Give the position of every Plasmodium parasite visible.
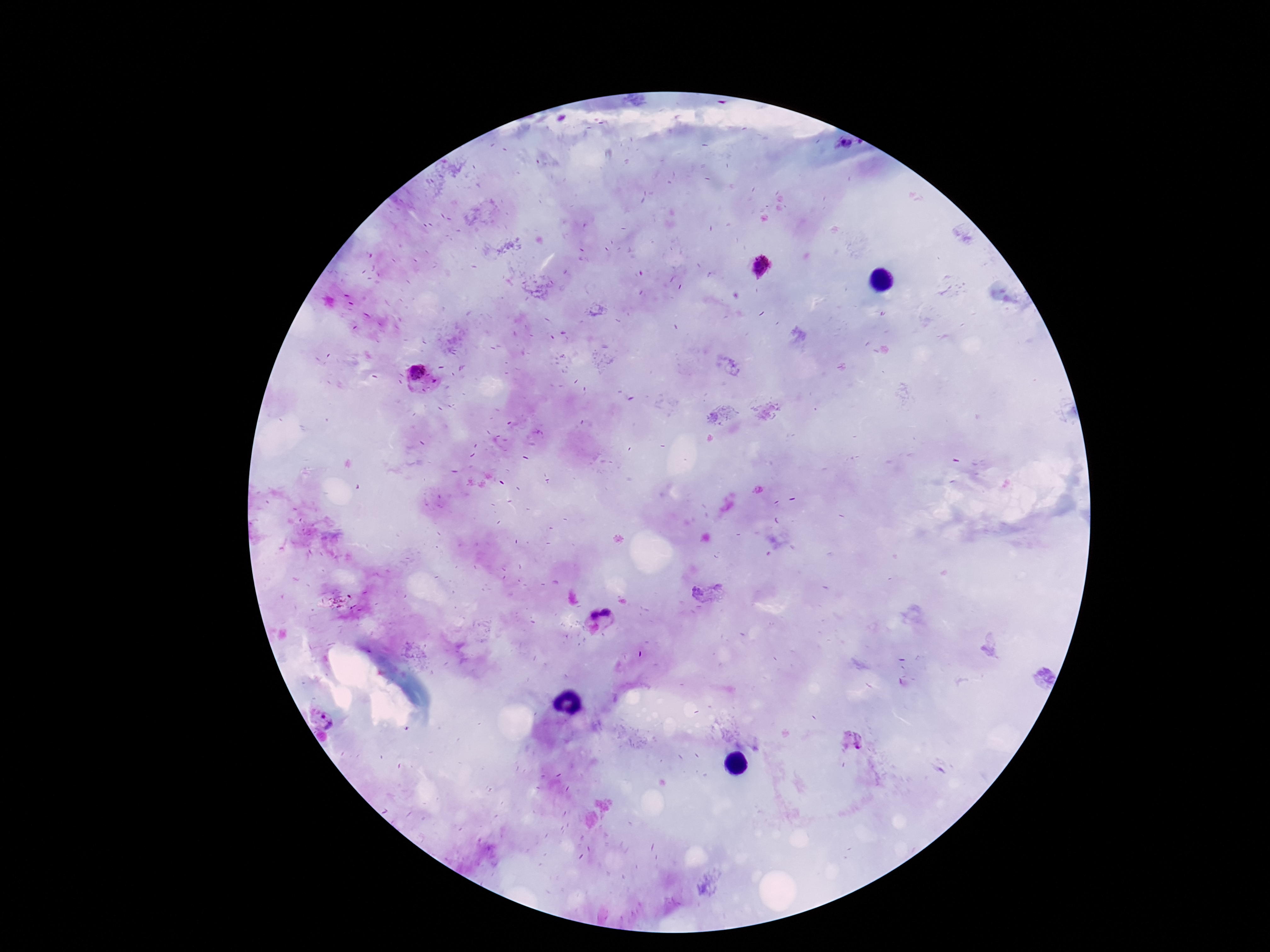
Approximate centers as (x, y) in pixels.
Plasmodium parasites: (845, 146), (761, 267), (419, 378), (705, 591), (608, 612), (593, 616), (1044, 679), (323, 720), (854, 740).

Summary:
  - Stain: Giemsa
  - Capture: smartphone camera through the microscope eyepiece
  - Patient malaria status: positive
  - Preparation: thick peripheral-blood smear
  - Field of view: single
  - Magnification: 100x
  - Image size: 1270×952 pixels